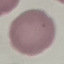
Summary:
  - Result: no malaria parasites detected
  - Capture: smartphone through the microscope eyepiece
  - Stain: Giemsa
  - Image type: automatically extracted cell patch, resized to 64 × 64 pixels
  - Preparation: thin blood film